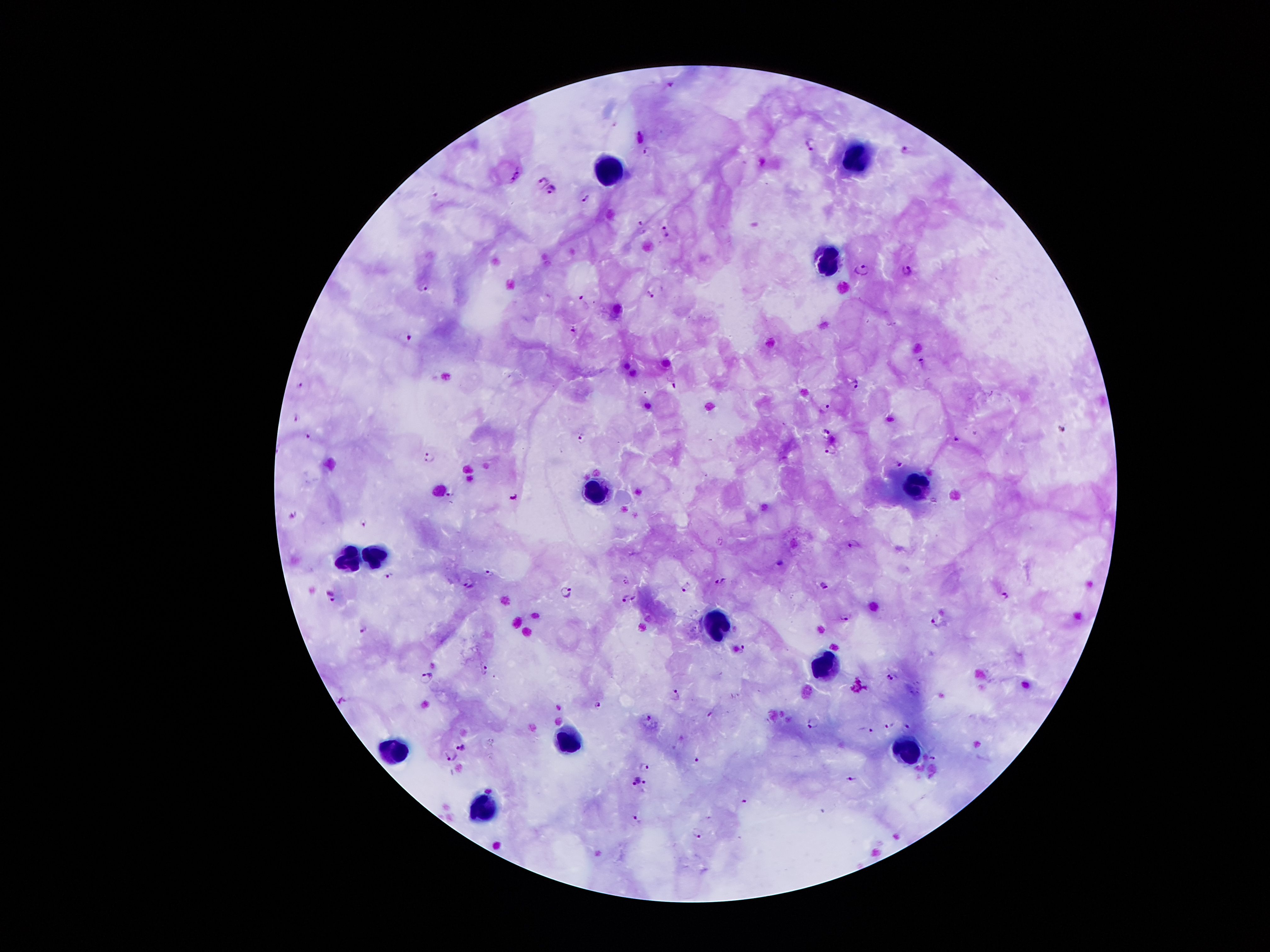

coordinate format = approximate object centers, in pixels from the top-left corner
malaria parasite locations = (x=671, y=83), (x=810, y=144), (x=906, y=149), (x=647, y=151), (x=517, y=173), (x=543, y=178), (x=552, y=190), (x=588, y=197), (x=642, y=226), (x=666, y=231), (x=862, y=268), (x=906, y=270), (x=425, y=286), (x=651, y=294), (x=584, y=300), (x=573, y=330), (x=410, y=337), (x=922, y=360), (x=854, y=383), (x=299, y=385), (x=673, y=385), (x=828, y=407), (x=294, y=419), (x=826, y=432), (x=310, y=435), (x=580, y=436), (x=955, y=439), (x=830, y=450), (x=429, y=456), (x=899, y=463), (x=450, y=493), (x=514, y=494), (x=293, y=514), (x=364, y=522), (x=854, y=544), (x=778, y=561), (x=490, y=572), (x=389, y=575), (x=625, y=582), (x=721, y=583), (x=469, y=584), (x=824, y=585), (x=684, y=588), (x=567, y=590), (x=1006, y=596), (x=334, y=598), (x=628, y=599), (x=846, y=618), (x=937, y=618), (x=363, y=628), (x=742, y=649), (x=484, y=669), (x=892, y=675), (x=425, y=678), (x=676, y=694), (x=597, y=704), (x=710, y=714), (x=649, y=718), (x=814, y=722), (x=888, y=724), (x=907, y=727), (x=868, y=730), (x=462, y=746), (x=933, y=757), (x=697, y=758), (x=448, y=759), (x=645, y=766), (x=851, y=778), (x=634, y=780), (x=644, y=782), (x=744, y=800), (x=635, y=817), (x=697, y=832)
leukocyte locations = (x=856, y=157), (x=606, y=167), (x=827, y=256), (x=919, y=483), (x=598, y=490), (x=345, y=553), (x=376, y=554), (x=718, y=623), (x=825, y=670), (x=564, y=742), (x=907, y=752), (x=396, y=753), (x=481, y=807)
preparation = thick blood film
magnification = 100x
capture = smartphone camera through the microscope eyepiece
stain = Giemsa
field of view = single
image size = 1270×952 pixels
patient malaria status = infected with Plasmodium falciparum